Give the position of every leukocyte visible.
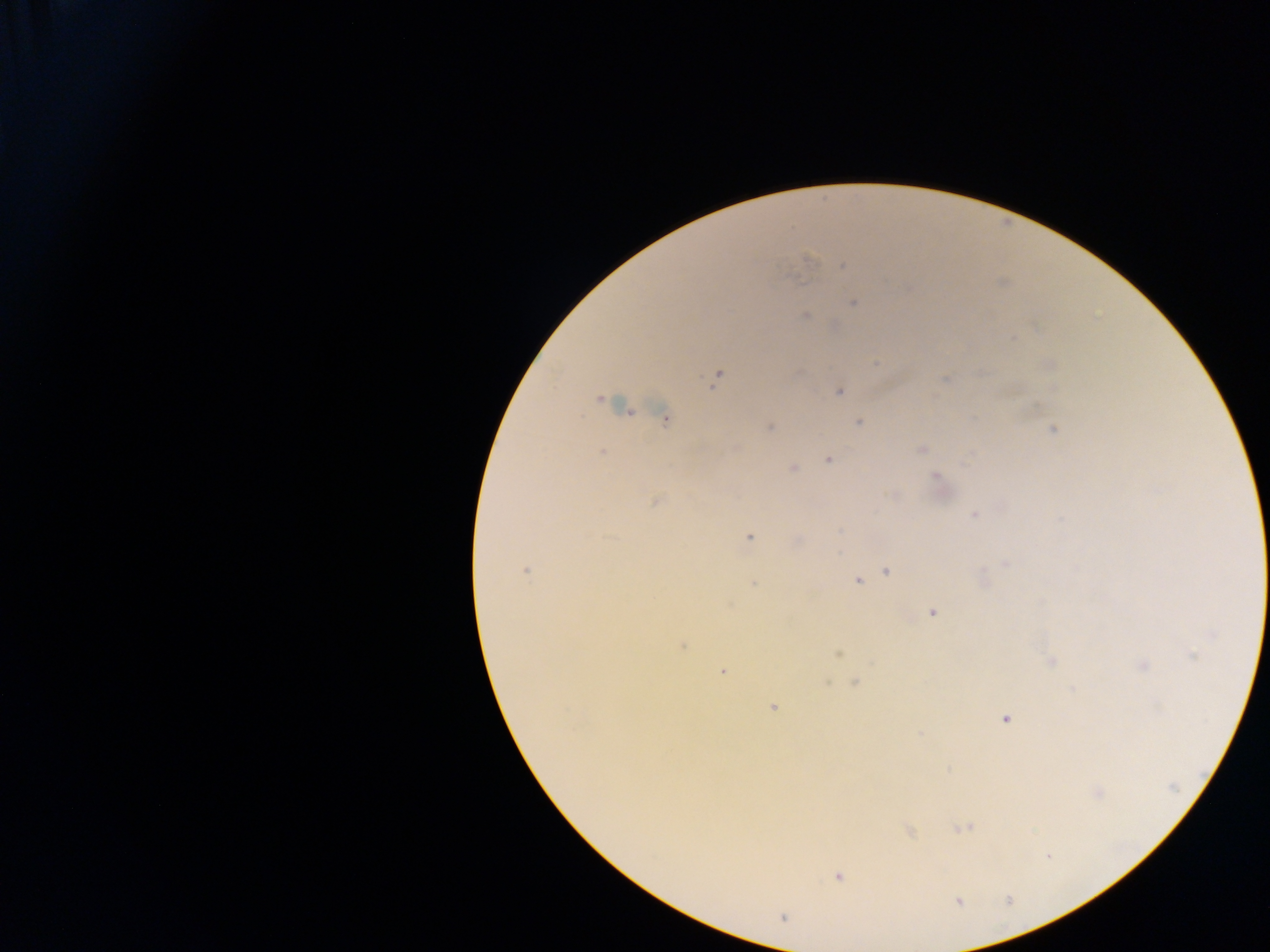

No leukocytes observed.

Approximate centers as {x, y} in pixels. Plasmodium parasite locations: {809, 259}, {843, 265}, {854, 303}, {805, 316}, {1013, 337}, {875, 363}, {716, 377}, {946, 380}, {839, 391}, {600, 399}, {665, 419}, {859, 421}, {770, 428}, {1052, 430}, {922, 450}, {602, 452}, {828, 459}, {793, 468}, {935, 476}, {656, 501}, {973, 514}, {749, 537}, {1005, 563}, {526, 571}, {887, 572}, {857, 581}, {753, 584}, {933, 612}, {1212, 635}, {682, 646}, {838, 653}, {1050, 661}, {1142, 665}, {722, 671}, {855, 682}, {773, 707}, {1005, 718}, {921, 733}, {1173, 787}, {964, 828}, {909, 831}, {838, 876}, {783, 917}. Single field of view. Image is 1270×952 pixels. Thick blood film. Collected in Ghana. Photographed through a microscope with a mobile-phone camera.